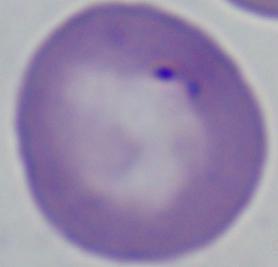
{
  "magnification": "1000x",
  "identification": "Babesia",
  "modality": "photomicrograph"
}